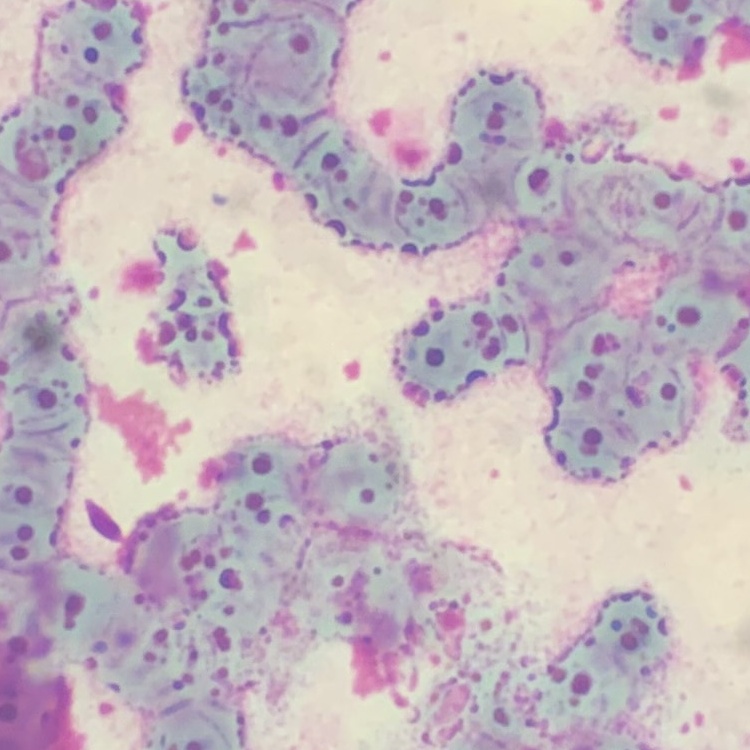
The red blood cells exhibit rouleaux formation. Thin blood smear. One tile cut from a larger photomicrograph. Field's or Giemsa stain.